Describe the morphology of the red blood cells.
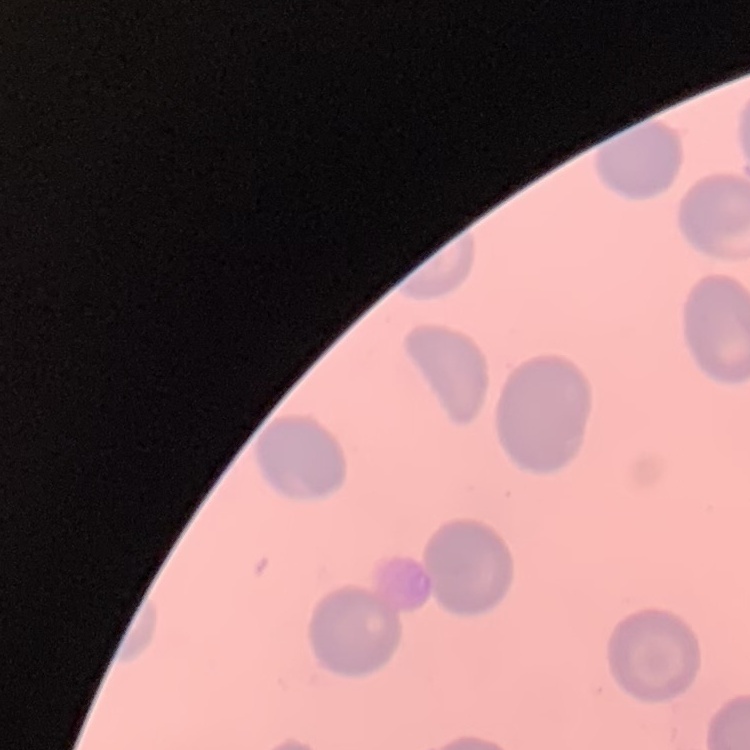

No rouleaux formation.

image type = one tile cut from a larger photomicrograph
preparation = thin blood smear
stain = Field's or Giemsa